Give the position of every malaria parasite.
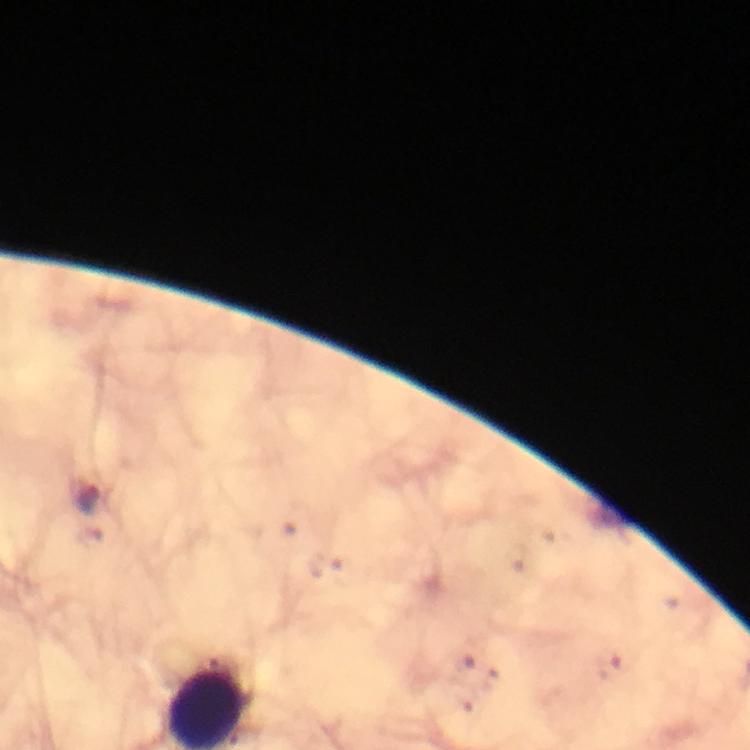

Approximate centers as {x, y} in pixels.
Malaria parasites: {88, 499}.

capture = smartphone photograph through a microscope
preparation = thick blood smear
stain = Giemsa
context = from a diagnostic examination for malaria
magnification = 100x
immersion oil = used
cropped from = a single field of view
image size = 750×750 pixels